Identify the cell.
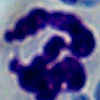
This is a leukocyte.

Summary:
  - Magnification: 1000x
  - Modality: photomicrograph